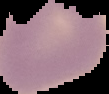
Summary:
  - Preparation: thin blood film
  - Image size: 109×94 pixels
  - Image type: segmented cell region on a black background
  - Malaria status: uninfected